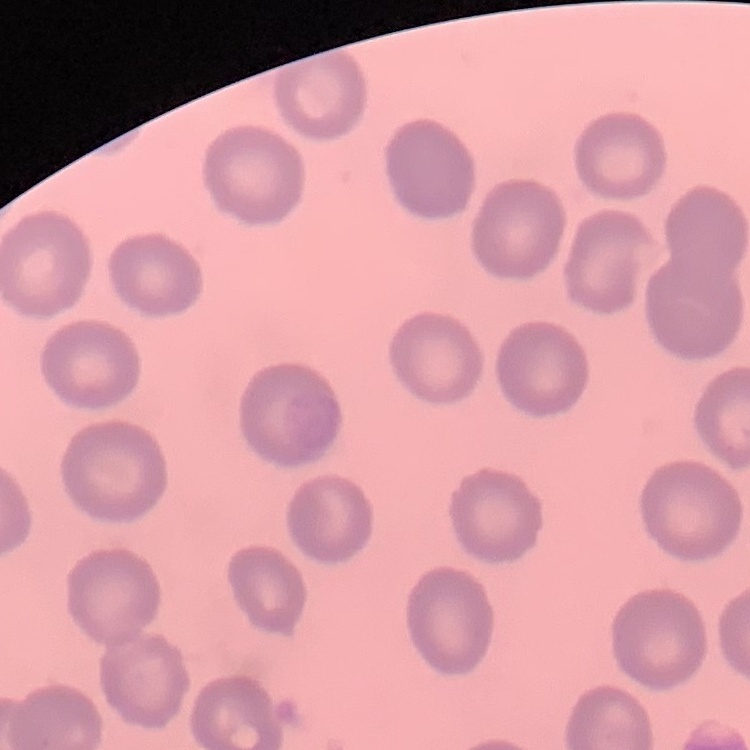 The red blood cells exhibit no rouleaux formation. Thin blood film. Stained with either Field's or Giemsa. One tile cut from a larger photomicrograph.